Give the position of every Plasmodium parasite.
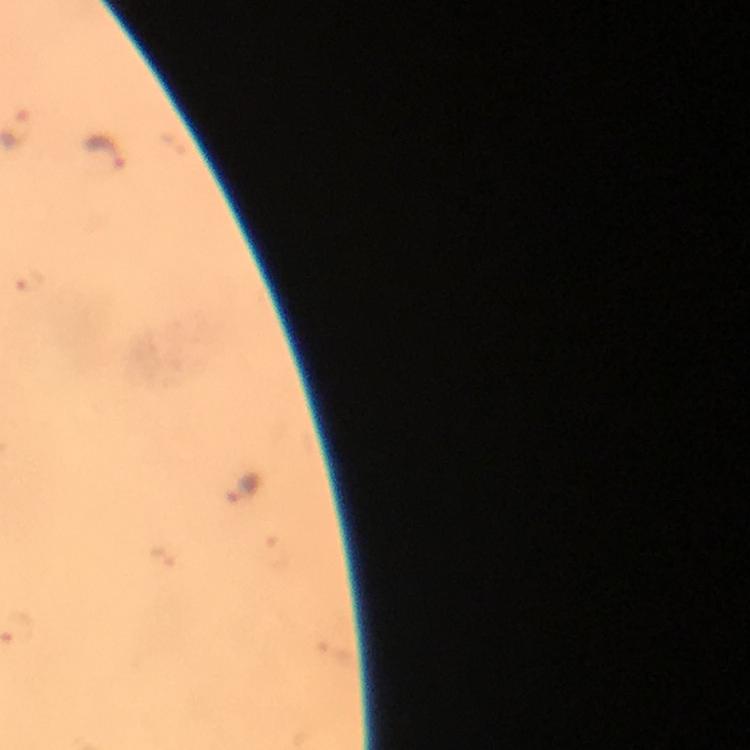
Approximate centers as [x, y] in pixels.
Plasmodium parasites: [102, 157], [28, 279], [243, 489].

context: from a diagnostic examination for malaria
immersion_oil: applied
magnification: 100x
preparation: thick smear
cropped_from: one field of view
stain: Giemsa
image_size: 750×750 pixels
capture: smartphone mounted on the microscope